Classify this cell by malaria status.
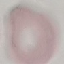
It is uninfected.

Summary:
  - Image type: automatically extracted cell patch, resized to 64 × 64 pixels
  - Stain: Giemsa
  - Capture: smartphone through the microscope eyepiece
  - Preparation: thin smear